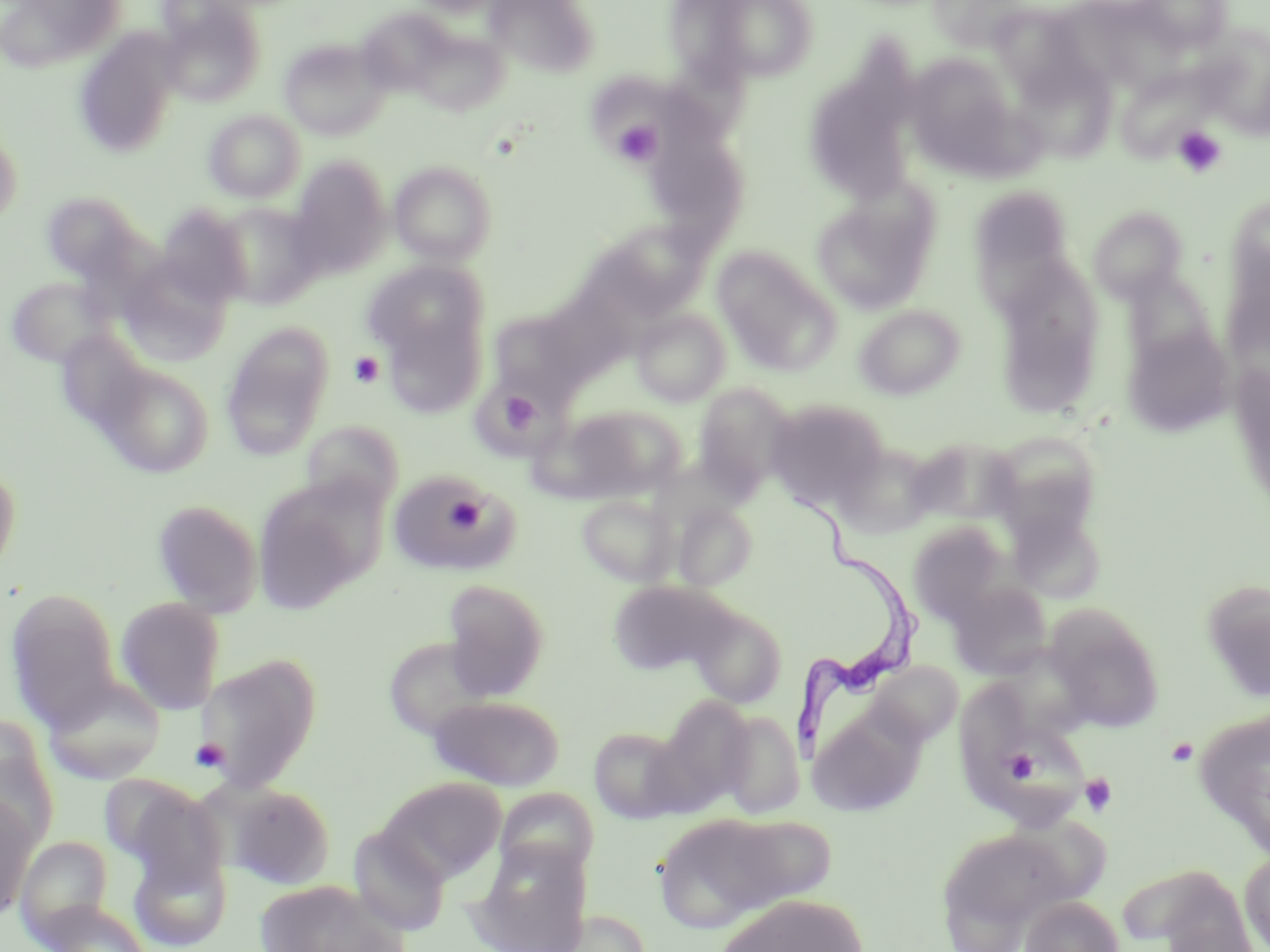 Approximate bounding boxes as [x1, y1, x2, y2] in pixels. Platelet locations: [612, 120, 663, 165], [1171, 125, 1227, 178], [348, 350, 385, 389], [493, 388, 544, 438], [443, 493, 485, 535], [1166, 737, 1199, 766], [190, 738, 231, 773], [1002, 750, 1037, 785], [1079, 772, 1117, 817]. Trypanosoma brucei locations: [784, 477, 928, 759]. Uninfected red blood cell locations: [2, 0, 128, 72], [485, 0, 598, 76], [710, 0, 818, 82], [929, 0, 1033, 52], [1134, 0, 1234, 53], [156, 1, 267, 107], [354, 14, 457, 92], [998, 17, 1094, 98], [412, 28, 509, 117], [1194, 28, 1270, 138], [72, 30, 182, 158], [279, 38, 392, 140], [904, 53, 1019, 164], [1025, 66, 1120, 170], [1116, 66, 1217, 162], [590, 69, 726, 164], [809, 78, 919, 201], [203, 110, 305, 204], [0, 130, 22, 226], [649, 140, 756, 236], [389, 160, 497, 265], [288, 161, 392, 280], [969, 185, 1075, 294], [811, 189, 940, 315], [42, 191, 143, 283], [1228, 193, 1270, 296], [211, 201, 323, 309], [157, 205, 252, 308], [1088, 207, 1186, 304], [578, 222, 707, 328], [713, 246, 840, 375], [118, 254, 234, 366], [984, 256, 1107, 339], [362, 261, 489, 368], [1120, 267, 1220, 372], [8, 277, 114, 368], [854, 304, 966, 400], [381, 306, 488, 419], [488, 308, 588, 400], [632, 309, 731, 407], [1010, 313, 1096, 416], [220, 322, 334, 460], [1123, 323, 1235, 438], [55, 329, 150, 433], [98, 362, 214, 477], [693, 383, 795, 496], [766, 399, 889, 509], [556, 404, 685, 502], [300, 419, 404, 515], [987, 430, 1104, 539], [909, 436, 1020, 526], [833, 442, 939, 538], [0, 461, 22, 582], [387, 472, 520, 576], [252, 476, 381, 613], [576, 495, 678, 586], [152, 500, 264, 618], [672, 501, 758, 590], [1004, 510, 1104, 605], [906, 520, 1013, 626], [440, 579, 550, 700], [947, 579, 1052, 680], [607, 580, 734, 676], [1202, 580, 1270, 704], [5, 588, 121, 730], [115, 598, 225, 714], [689, 602, 788, 708], [1045, 606, 1165, 733], [382, 636, 496, 741], [194, 652, 323, 793], [866, 662, 962, 748], [42, 675, 166, 785], [961, 682, 1051, 803], [426, 694, 566, 790], [656, 695, 756, 811], [809, 708, 924, 816], [1194, 709, 1270, 857], [717, 710, 805, 818], [0, 718, 60, 848], [588, 726, 689, 824], [994, 729, 1091, 832], [378, 777, 506, 882], [107, 778, 230, 894], [225, 783, 337, 889], [494, 787, 598, 884], [0, 794, 40, 920], [652, 813, 813, 934], [711, 814, 839, 910], [936, 826, 1074, 947], [348, 828, 450, 936], [15, 836, 114, 944], [469, 839, 592, 952], [128, 844, 232, 951], [1239, 850, 1270, 951], [1119, 863, 1255, 949], [252, 880, 403, 952], [717, 894, 866, 951], [1021, 895, 1124, 952], [40, 900, 154, 952], [573, 909, 651, 952]. Slide-level diagnosis: Trypanosoma brucei. Single field of view. May-Grünwald-Giemsa stain. Light microscopy. Thin blood film. Captured at 1000x magnification. Image is 1270×952 pixels.